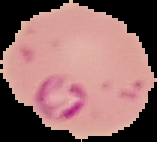
Summary:
  - Image size: 157×142 pixels
  - Image type: segmented cell region with the area outside set to black
  - Preparation: thin blood film
  - Malaria status: parasitized